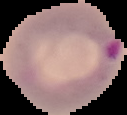

preparation: thin blood smear
image_type: segmented cell region on a black background
malaria_status: parasitized
image_size: 127×115 pixels